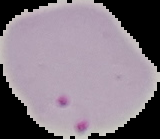
Summary:
  - Image type: segmented cell region on a black background
  - Malaria status: parasitized
  - Preparation: thin blood film
  - Image size: 160×139 pixels